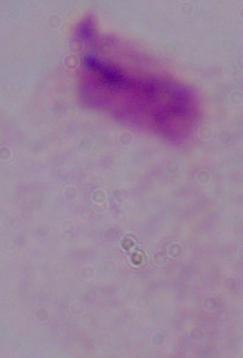
identification = trichomonad
magnification = 1000x
modality = photomicrograph